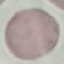 Malaria status: uninfected. Automatically extracted cell patch, resized to 64 × 64 pixels. Thin blood smear. Photographed with a smartphone camera at the microscope eyepiece. Giemsa stain.